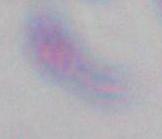

Summary:
  - Modality: photomicrograph
  - Identification: Toxoplasma gondii
  - Magnification: 1000x